Report the malaria status of this cell.
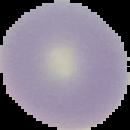

Uninfected.

Image is 130×130 pixels. Cell region segmented out of the field of view; the surrounding area is masked to black. From a thin blood smear.